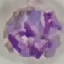

Summary:
  - Result: malaria parasites detected
  - Image type: automatically extracted cell patch, resized to 64 × 64 pixels
  - Preparation: thin smear
  - Capture: smartphone through the microscope eyepiece
  - Stain: Giemsa